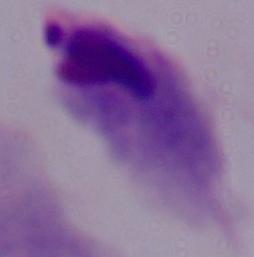

Micrograph. 1000x magnification. A trichomonad is seen.